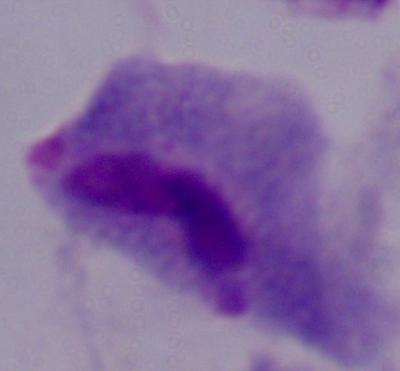

Captured at 1000x magnification. A trichomonad is shown. Micrograph.